Classify this cell by malaria status.
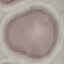
It is uninfected.

Summary:
  - Capture: smartphone through the microscope eyepiece
  - Preparation: thin blood smear
  - Image type: automatically extracted cell patch, resized to 64 × 64 pixels
  - Stain: Giemsa